Name the cell type shown.
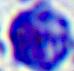
This is a leukocyte.

Summary:
  - Modality: photomicrograph
  - Magnification: 400x